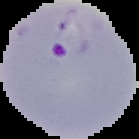
Segmented cell region on a black background. From a thin blood film. Image is 139×139 pixels. Malaria status: parasitized.